Name the blood parasite species.
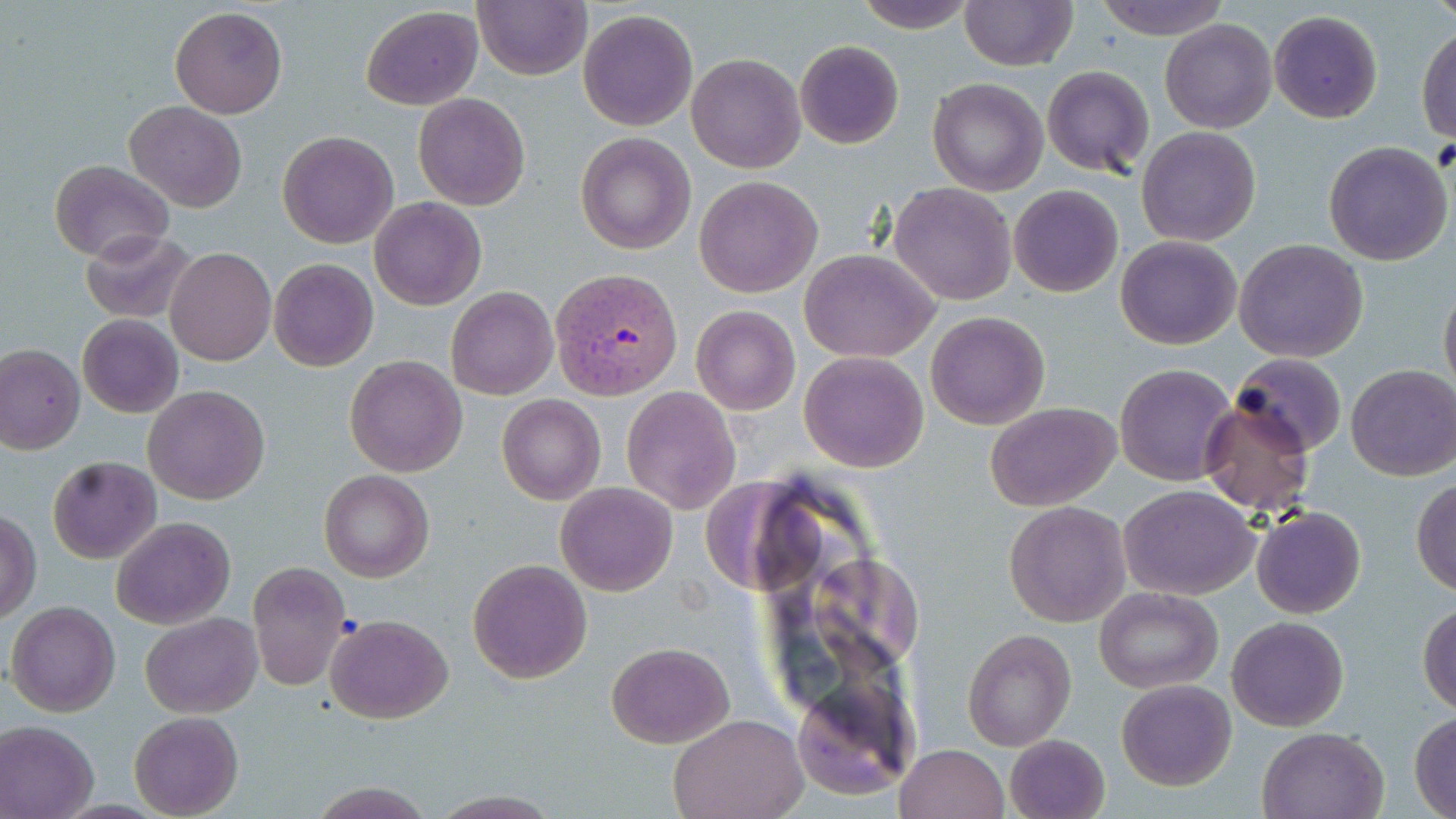

Plasmodium vivax.

Approximate bounding boxes as named x1/y1/x2/y2 corners in pixels. Plasmodium vivax-infected red blood cell locations: (x1=549, y1=266, x2=681, y2=397). Uninfected red blood cell locations: (x1=473, y1=0, x2=592, y2=80), (x1=852, y1=0, x2=978, y2=32), (x1=958, y1=0, x2=1077, y2=70), (x1=1093, y1=0, x2=1233, y2=39), (x1=169, y1=6, x2=288, y2=117), (x1=360, y1=6, x2=482, y2=110), (x1=577, y1=8, x2=699, y2=132), (x1=1268, y1=10, x2=1383, y2=123), (x1=1158, y1=19, x2=1278, y2=134), (x1=1416, y1=23, x2=1456, y2=144), (x1=794, y1=40, x2=904, y2=149), (x1=686, y1=54, x2=807, y2=173), (x1=1042, y1=66, x2=1156, y2=177), (x1=928, y1=78, x2=1048, y2=195), (x1=413, y1=93, x2=530, y2=210), (x1=126, y1=101, x2=246, y2=212), (x1=1135, y1=126, x2=1260, y2=248), (x1=276, y1=131, x2=399, y2=247), (x1=576, y1=132, x2=695, y2=254), (x1=1324, y1=141, x2=1454, y2=266), (x1=50, y1=160, x2=173, y2=261), (x1=694, y1=176, x2=822, y2=297), (x1=889, y1=183, x2=1016, y2=304), (x1=1009, y1=186, x2=1123, y2=297), (x1=370, y1=197, x2=487, y2=310), (x1=79, y1=229, x2=194, y2=323), (x1=1115, y1=236, x2=1241, y2=350), (x1=1234, y1=238, x2=1368, y2=363), (x1=167, y1=246, x2=277, y2=366), (x1=799, y1=248, x2=940, y2=363), (x1=269, y1=258, x2=378, y2=371), (x1=1439, y1=278, x2=1456, y2=398), (x1=447, y1=288, x2=557, y2=400), (x1=691, y1=304, x2=801, y2=415), (x1=925, y1=310, x2=1050, y2=429), (x1=78, y1=314, x2=184, y2=419), (x1=0, y1=344, x2=84, y2=453), (x1=799, y1=351, x2=929, y2=473), (x1=1228, y1=352, x2=1348, y2=456), (x1=345, y1=355, x2=468, y2=477), (x1=1115, y1=363, x2=1236, y2=485), (x1=1347, y1=365, x2=1456, y2=481), (x1=144, y1=385, x2=271, y2=504), (x1=622, y1=386, x2=740, y2=513), (x1=497, y1=394, x2=605, y2=505), (x1=1199, y1=398, x2=1317, y2=516), (x1=984, y1=401, x2=1122, y2=513), (x1=47, y1=457, x2=160, y2=564), (x1=318, y1=468, x2=433, y2=582), (x1=1411, y1=478, x2=1456, y2=597), (x1=555, y1=482, x2=678, y2=596), (x1=1118, y1=484, x2=1261, y2=599), (x1=1003, y1=501, x2=1131, y2=627), (x1=1250, y1=506, x2=1365, y2=619), (x1=1, y1=509, x2=40, y2=621), (x1=112, y1=517, x2=235, y2=628), (x1=467, y1=558, x2=592, y2=684), (x1=247, y1=561, x2=351, y2=690), (x1=1093, y1=586, x2=1223, y2=693), (x1=6, y1=601, x2=121, y2=718), (x1=1419, y1=602, x2=1456, y2=715), (x1=326, y1=612, x2=453, y2=722), (x1=141, y1=613, x2=261, y2=717), (x1=1228, y1=615, x2=1348, y2=730), (x1=963, y1=627, x2=1075, y2=751), (x1=607, y1=643, x2=731, y2=747), (x1=1115, y1=680, x2=1237, y2=789), (x1=790, y1=688, x2=915, y2=803), (x1=129, y1=711, x2=243, y2=819), (x1=667, y1=711, x2=808, y2=819), (x1=1409, y1=712, x2=1455, y2=818), (x1=0, y1=721, x2=98, y2=819), (x1=1257, y1=726, x2=1388, y2=818), (x1=1004, y1=734, x2=1110, y2=819), (x1=895, y1=744, x2=1010, y2=819). 1000x magnification. Image is 1456×819 pixels. May-Grünwald-Giemsa stain. Thin blood film. Light microscopy. One field of a larger specimen.